State which parasite is depicted.
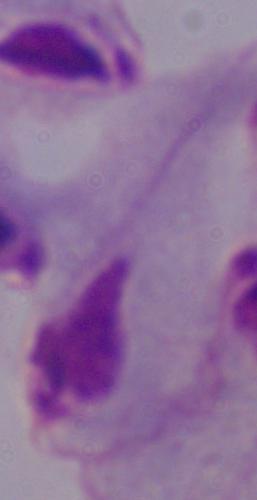
This is a trichomonad.

Photomicrograph. Captured at 1000x magnification.